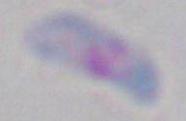
Toxoplasma gondii is seen. Captured at 1000x magnification. Photomicrograph.